Describe the morphology of the erythrocytes.
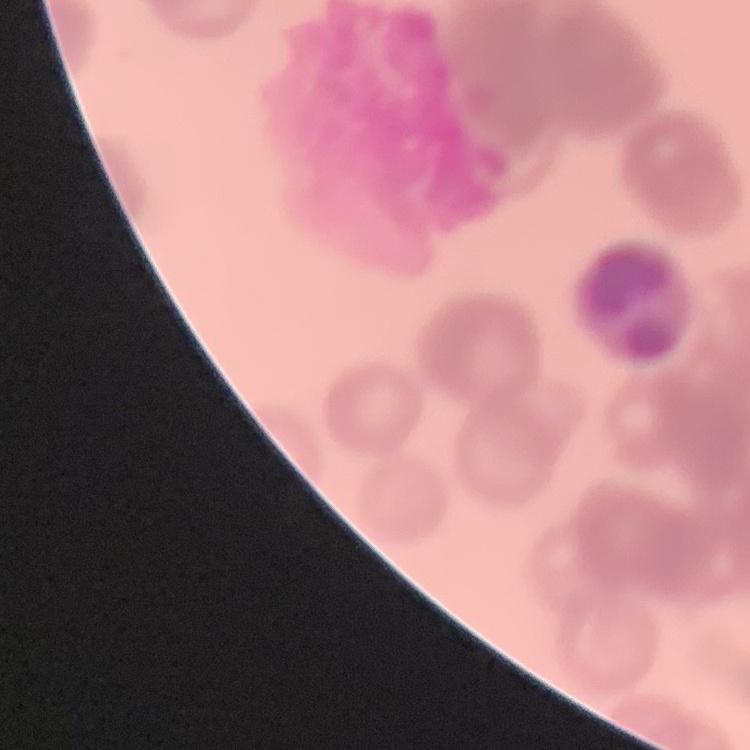

They show rouleaux formation.

image type = one tile cut from a larger photomicrograph
stain = Field's or Giemsa
preparation = thin blood film